Identify the blood parasite species.
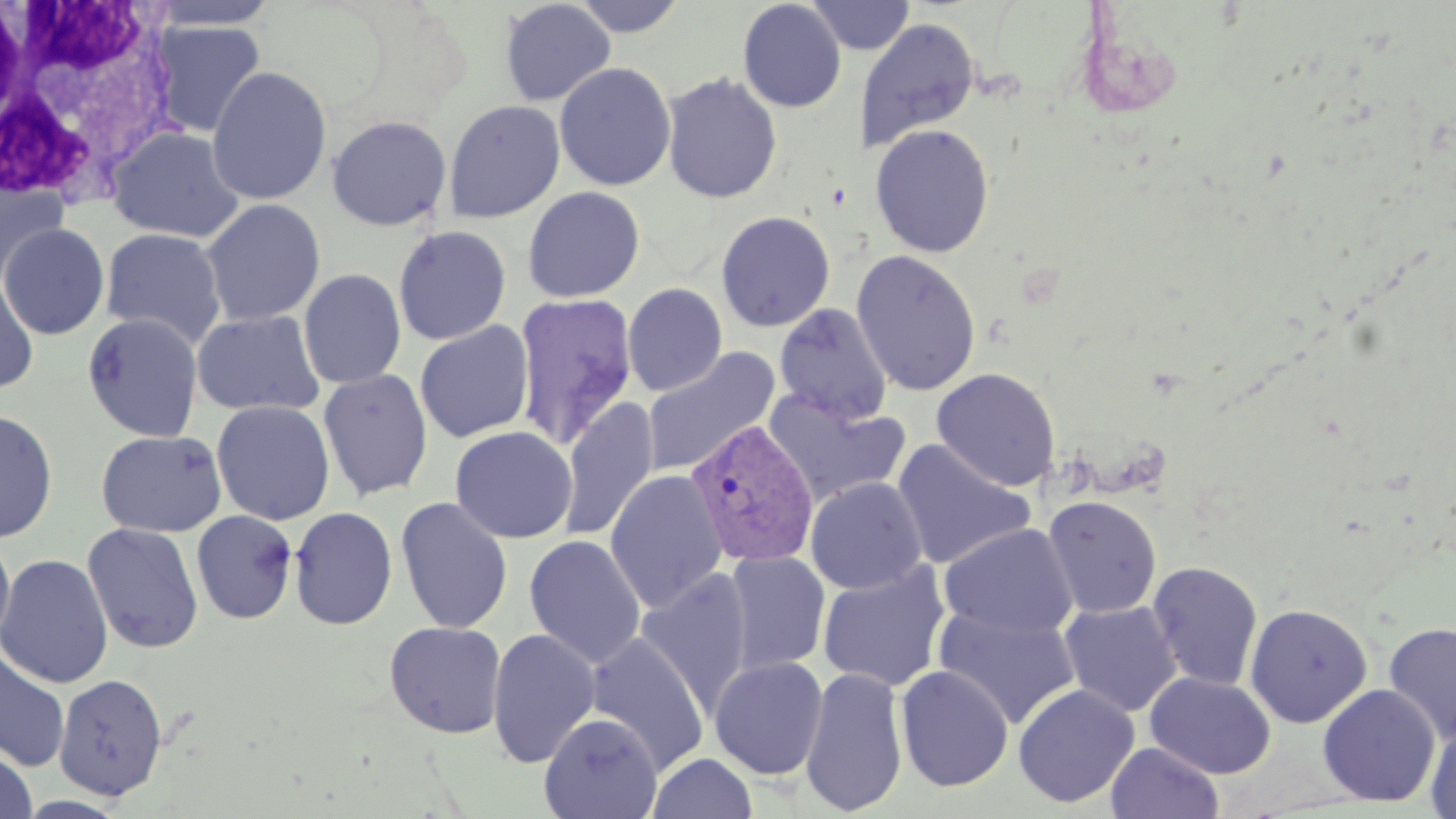

Plasmodium vivax.

modality: optical microscopy
white_blood_cell_locations: 'approximate bounding boxes as (x1, y1, x2, y2) in pixels: (1, 0, 181, 210)'
plasmodium_vivax_infected_red_blood_cell_locations: 'approximate bounding boxes as (x1, y1, x2, y2) in pixels: (685, 418, 820, 568)'
field_of_view: single
preparation: thin blood film
image_size: 1456×819 pixels
magnification: 1000x
uninfected_red_blood_cell_locations: 'approximate bounding boxes as (x1, y1, x2, y2) in pixels: (147, 0, 279, 30), (570, 0, 688, 37), (805, 0, 916, 55), (500, 1, 616, 106), (737, 1, 847, 113), (855, 18, 979, 153), (149, 20, 265, 139), (554, 62, 676, 192), (207, 66, 331, 205), (661, 72, 782, 204), (443, 100, 565, 223), (327, 115, 452, 231), (870, 124, 994, 258), (107, 127, 244, 242), (0, 175, 68, 288), (522, 186, 645, 302), (201, 199, 326, 326), (716, 211, 835, 332), (0, 223, 110, 340), (392, 225, 511, 344), (100, 227, 227, 350), (851, 249, 981, 396), (298, 269, 406, 389), (0, 273, 39, 394), (623, 283, 728, 396), (513, 293, 638, 452), (774, 303, 893, 425), (191, 309, 325, 417), (82, 313, 203, 442), (415, 321, 534, 443), (642, 347, 781, 477), (318, 368, 433, 501), (931, 368, 1061, 491), (763, 389, 910, 508), (558, 398, 660, 543), (211, 400, 335, 525), (0, 409, 59, 543), (450, 426, 578, 544), (95, 430, 227, 537), (891, 438, 1035, 570), (605, 470, 728, 614), (806, 477, 927, 595), (395, 496, 513, 634), (1042, 496, 1162, 618), (289, 506, 398, 630), (191, 510, 298, 625), (938, 522, 1078, 640), (82, 523, 204, 654), (0, 531, 16, 653), (524, 535, 646, 668), (724, 550, 831, 676), (1, 554, 114, 689), (817, 560, 951, 692), (1147, 561, 1263, 691), (636, 568, 753, 718), (1059, 600, 1183, 717), (1245, 603, 1372, 728), (932, 604, 1083, 730), (383, 621, 507, 738), (1383, 621, 1456, 744), (486, 627, 601, 768), (584, 631, 711, 776), (0, 649, 70, 772), (709, 656, 828, 780), (895, 665, 1014, 792), (799, 666, 909, 816), (1145, 671, 1276, 779), (53, 673, 168, 800), (1013, 683, 1139, 808), (1317, 684, 1441, 807), (539, 712, 663, 819), (1424, 720, 1456, 819), (1106, 742, 1224, 819), (0, 748, 38, 819), (648, 752, 757, 819)'
stain: May-Grünwald-Giemsa